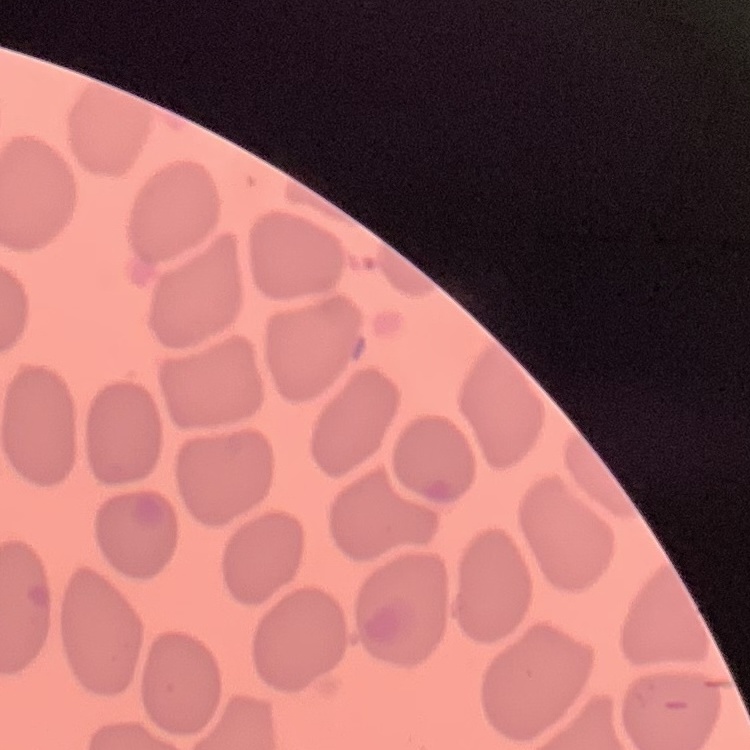
The erythrocytes exhibit no rouleaux formation. Square crop of a larger photomicrograph. Thin blood film. Stained with either Field's or Giemsa.